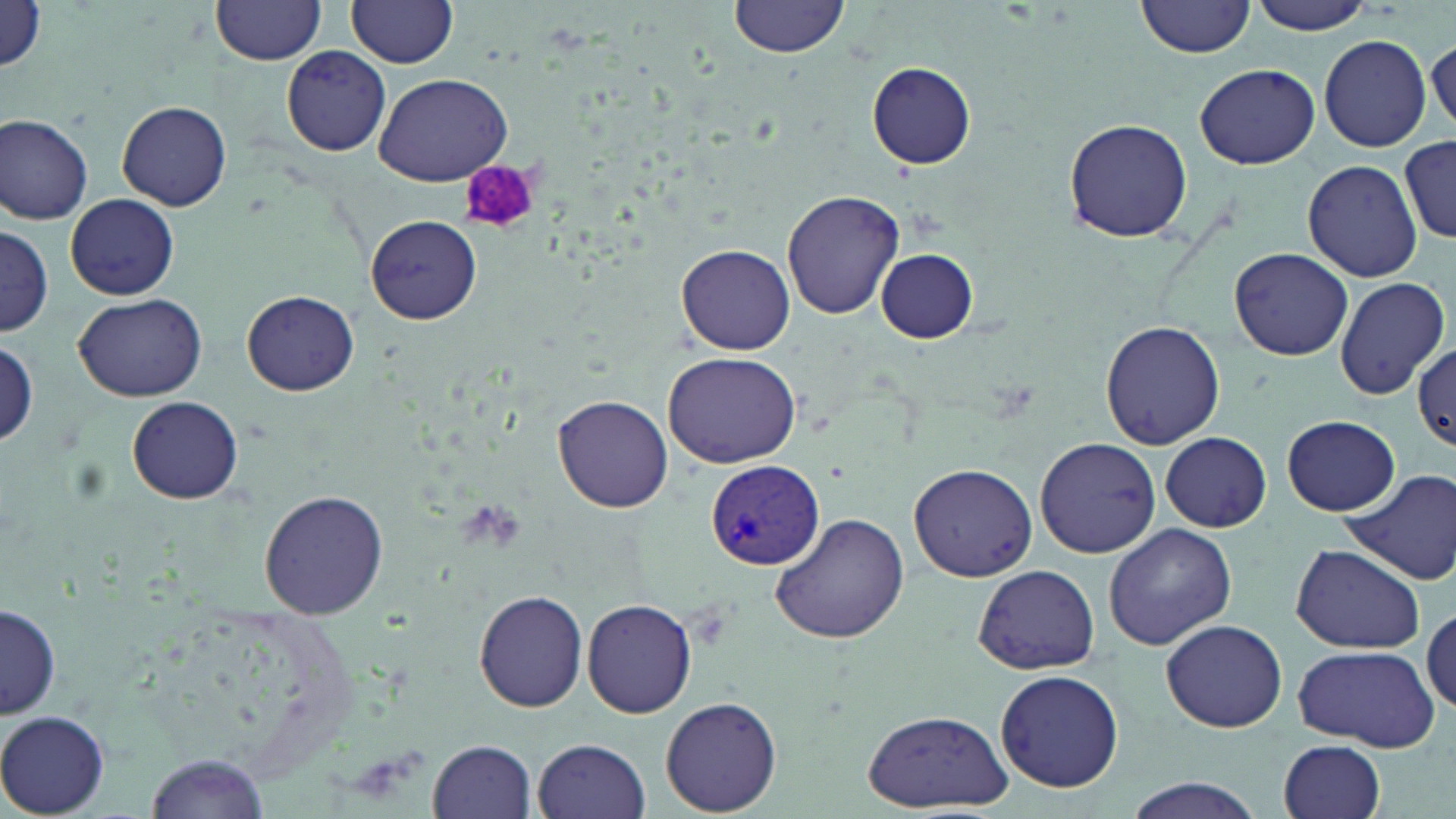

Summary:
  - Coordinate format: approximate bounding boxes as (x1,y1)-(x2,y2) corner pairs in pixels
  - Uninfected red blood cell locations: (730,0)-(848,58), (1138,0)-(1255,58), (1247,0)-(1381,33), (210,1)-(324,67), (348,1)-(458,69), (1,3)-(49,75), (1319,34)-(1431,153), (1427,38)-(1456,138), (281,45)-(392,157), (1316,49)-(1429,259), (867,63)-(977,168), (1195,64)-(1319,169), (374,73)-(513,186), (117,102)-(231,210), (0,112)-(93,225), (1062,118)-(1196,242), (1401,137)-(1455,244), (1303,159)-(1424,282), (781,189)-(905,320), (65,194)-(179,300), (366,215)-(481,323), (0,222)-(53,338), (677,244)-(797,354), (1231,248)-(1353,360), (875,249)-(978,342), (1333,277)-(1449,399), (241,290)-(360,396), (73,292)-(207,402), (1099,320)-(1224,449), (0,338)-(40,447), (1411,344)-(1456,450), (662,351)-(804,466), (553,395)-(673,512), (126,396)-(243,504), (1283,416)-(1399,515), (1292,427)-(1443,556), (1160,433)-(1271,531), (1032,436)-(1162,558), (910,465)-(1036,580), (1340,468)-(1456,585), (259,489)-(389,619), (772,511)-(913,645), (1103,523)-(1238,651), (1289,543)-(1427,654), (972,564)-(1100,676), (474,588)-(589,713), (583,599)-(699,719), (1,601)-(61,718), (1423,604)-(1456,714), (1160,617)-(1288,733), (1293,643)-(1438,752), (994,669)-(1124,792), (660,696)-(783,815), (860,707)-(1015,812), (0,709)-(113,815), (533,738)-(650,819), (427,739)-(537,819), (1278,739)-(1387,819), (147,752)-(271,817), (1121,779)-(1264,819)
  - Plasmodium vivax-infected red blood cell locations: (704,459)-(826,571)
  - Platelet locations: (459,162)-(541,236)
  - Slide-level diagnosis: Plasmodium vivax
  - Magnification: 1000x
  - Stain: May-Grünwald-Giemsa
  - Field of view: single
  - Image size: 1456×819 pixels
  - Modality: optical microscopy
  - Preparation: thin blood film